Identify the parasite.
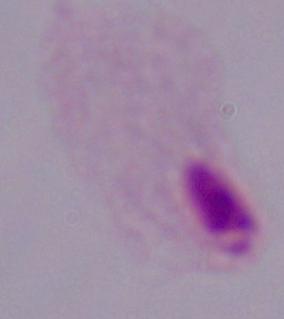
A trichomonad.

Photomicrograph. 1000x magnification.